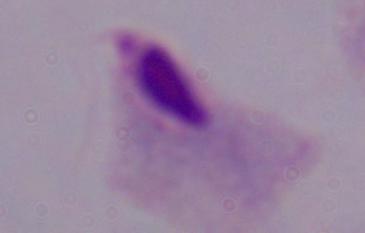

Summary:
  - Identification: trichomonad
  - Magnification: 1000x
  - Modality: micrograph